Point out each Plasmodium parasite.
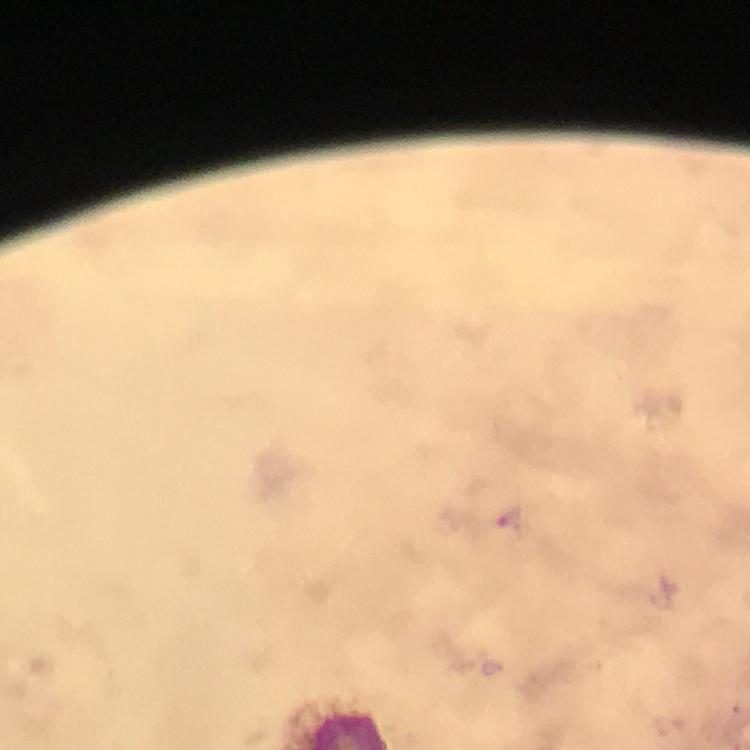

Approximate object centers, in pixels from the top-left corner.
Plasmodium parasites: (x=508, y=519).

From a diagnostic examination for malaria. Immersion oil was used. Smartphone photograph taken through a microscope. Thick smear. Image is 750×750 pixels. At 100x magnification. Giemsa stain. A crop from one field of view.